State which parasite is depicted.
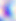

This is Toxoplasma gondii.

Micrograph. 400x magnification.